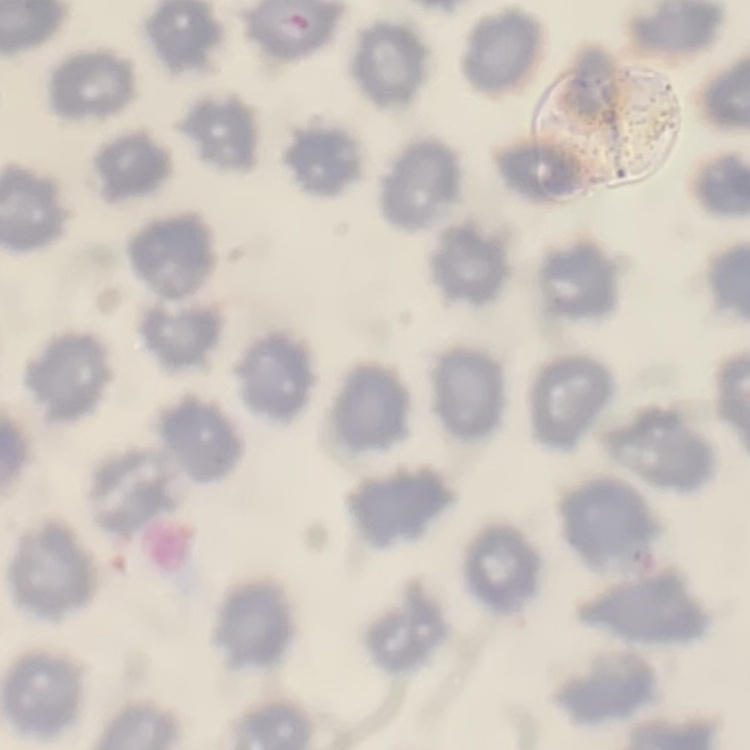
Summary:
  - Erythrocyte morphology: no rouleaux formation
  - Image type: one tile cut from a larger photomicrograph
  - Stain: Field's or Giemsa
  - Preparation: thin peripheral smear